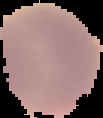
The area outside the segmented cell region is set to black. Image is 103×118 pixels. From a thin blood smear. Malaria status: uninfected.